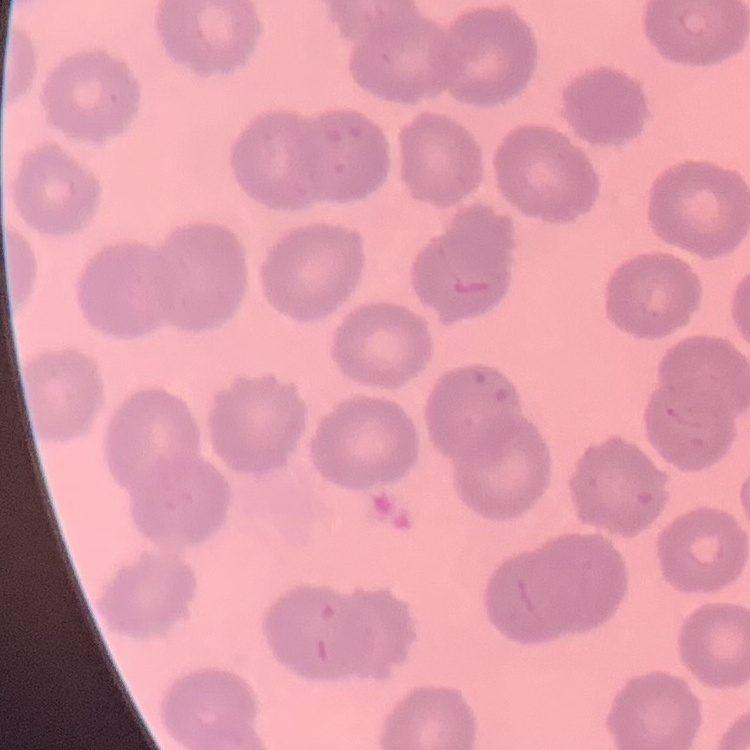

The red blood cells show no rouleaux formation. Field's or Giemsa stain. Square crop of a larger photomicrograph. Thin peripheral smear.